Assess this cell for malaria.
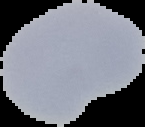

It is uninfected.

Summary:
  - Image type: segmented cell region with the area outside set to black
  - Preparation: thin blood film
  - Image size: 145×127 pixels